Classify this cell by malaria status.
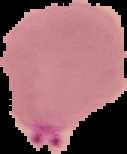
It is parasitized.

Summary:
  - Image size: 127×154 pixels
  - Preparation: thin blood film
  - Image type: segmented cell region with the area outside set to black